Name the cell type shown.
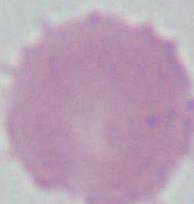

An erythrocyte.

Photomicrograph. 1000x magnification.